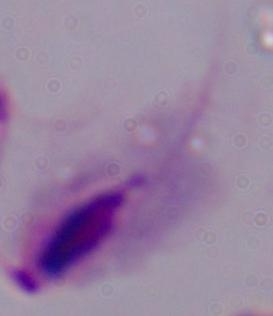

A trichomonad is seen. Micrograph. Captured at 1000x magnification.